Classify this cell by malaria status.
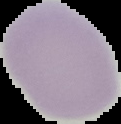
Uninfected.

Segmented cell region on a black background. Image is 121×124 pixels. From a thin blood film.